Report the malaria status of this cell.
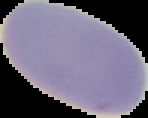
It is uninfected.

From a thin blood smear. Image is 148×118 pixels. Cell region segmented out of the field of view; the surrounding area is masked to black.